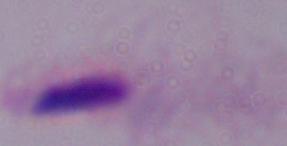
{
  "identification": "trichomonad",
  "magnification": "1000x",
  "modality": "micrograph"
}